Outline each uninfected red blood cell.
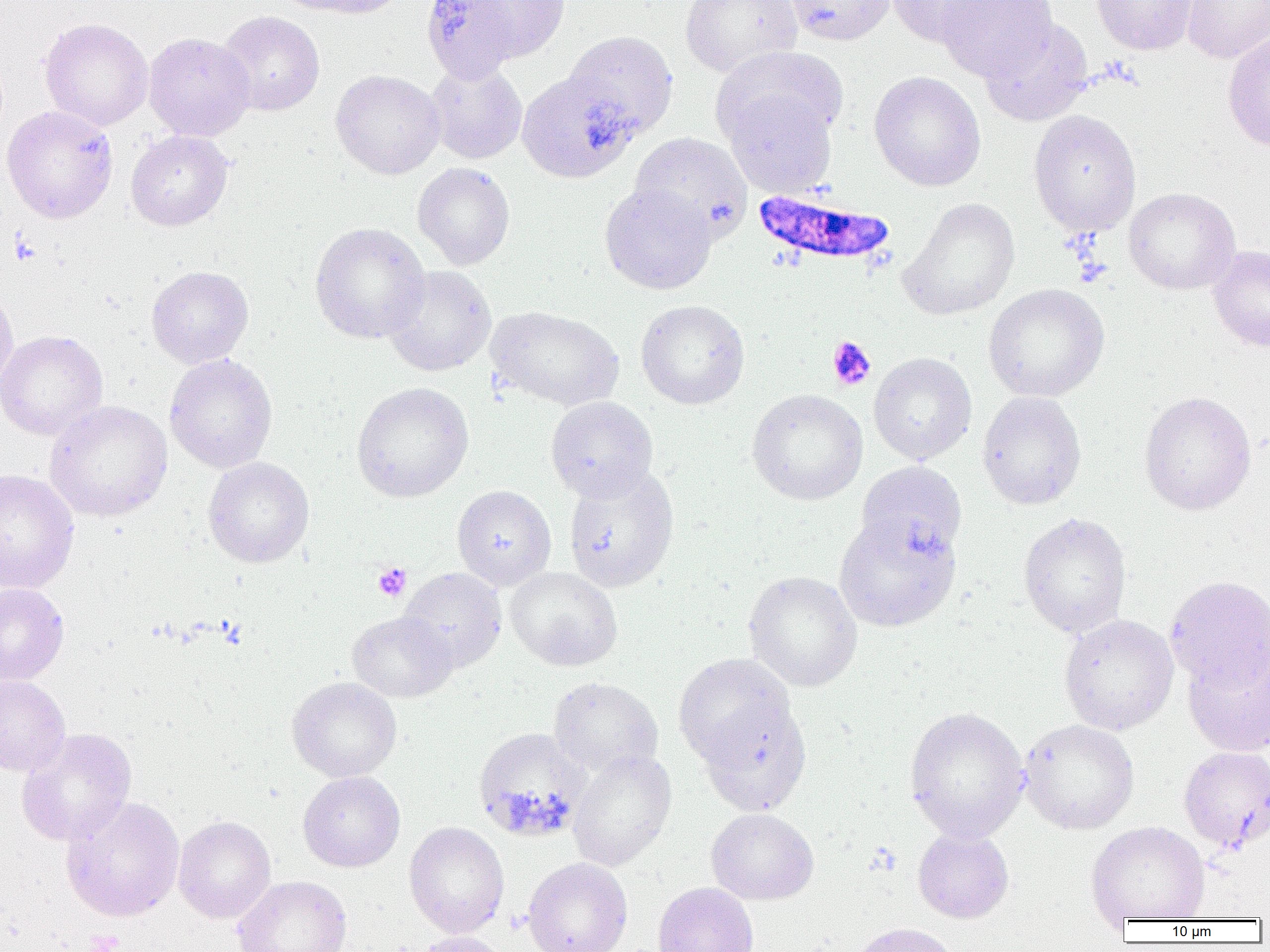

Approximate bounding boxes as (x1,y1)-(x2,y2) corner pairs in pixels.
Uninfected red blood cells: (274,0)-(407,19), (467,0)-(571,61), (680,0)-(802,77), (784,0)-(896,46), (884,0)-(1001,47), (936,0)-(1058,81), (1091,0)-(1200,55), (1181,0)-(1270,63), (421,1)-(519,83), (217,10)-(326,116), (39,18)-(153,131), (979,18)-(1093,127), (563,30)-(679,141), (1222,31)-(1270,151), (144,32)-(256,141), (712,45)-(849,150), (425,61)-(527,165), (330,69)-(445,179), (517,70)-(638,182), (869,71)-(986,192), (721,89)-(837,198), (2,105)-(118,224), (1028,109)-(1142,238), (125,129)-(234,231), (629,132)-(752,241), (412,162)-(516,270), (599,183)-(717,294), (1123,187)-(1241,295), (899,197)-(1020,321), (309,222)-(430,344), (1208,245)-(1270,352), (146,265)-(253,368), (382,265)-(496,376), (983,283)-(1110,402), (0,286)-(18,392), (635,299)-(750,409), (486,306)-(625,411), (0,330)-(108,440), (868,352)-(977,464), (164,354)-(278,474), (351,381)-(473,502), (747,389)-(868,505), (977,391)-(1087,510), (1139,391)-(1257,516), (545,396)-(658,502), (44,400)-(173,522), (203,457)-(314,567), (854,461)-(967,563), (563,465)-(679,593), (0,469)-(80,593), (452,485)-(556,590), (1018,512)-(1132,638), (833,513)-(962,632), (505,566)-(623,671), (398,567)-(507,672), (743,570)-(863,692), (1165,575)-(1270,692), (0,582)-(69,685), (347,611)-(456,702), (1058,614)-(1179,735), (1182,647)-(1270,756), (672,653)-(795,768), (0,675)-(71,776), (287,676)-(402,782), (548,676)-(663,779), (698,700)-(812,816), (904,706)-(1029,843), (1018,718)-(1139,834), (16,727)-(137,847), (473,727)-(591,842), (1179,746)-(1270,852), (568,749)-(677,872), (298,771)-(405,872), (60,796)-(185,922), (706,808)-(818,905), (173,816)-(276,923), (1086,820)-(1211,922), (404,821)-(509,938), (912,827)-(1014,923), (523,857)-(632,952), (233,875)-(352,952), (652,882)-(759,952), (849,922)-(959,952), (411,931)-(512,952).

slide-level diagnosis = Plasmodium falciparum
magnification = 1000x
modality = light microscopy
field of view = one of a larger specimen
platelet locations = approximate bounding boxes as (x1,y1)-(x2,y2) corner pairs in pixels: (8,233)-(41,265), (826,336)-(876,391), (372,563)-(411,601), (84,930)-(124,952)
image size = 1270×952 pixels
preparation = thin blood film
Plasmodium falciparum-infected red blood cell locations = approximate bounding boxes as (x1,y1)-(x2,y2) corner pairs in pixels: (752,189)-(897,269)